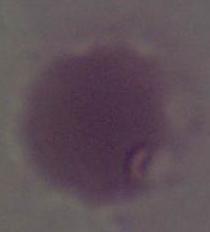 Micrograph. 1000x magnification. An erythrocyte is shown.